Outline each blood parasite and name the species.
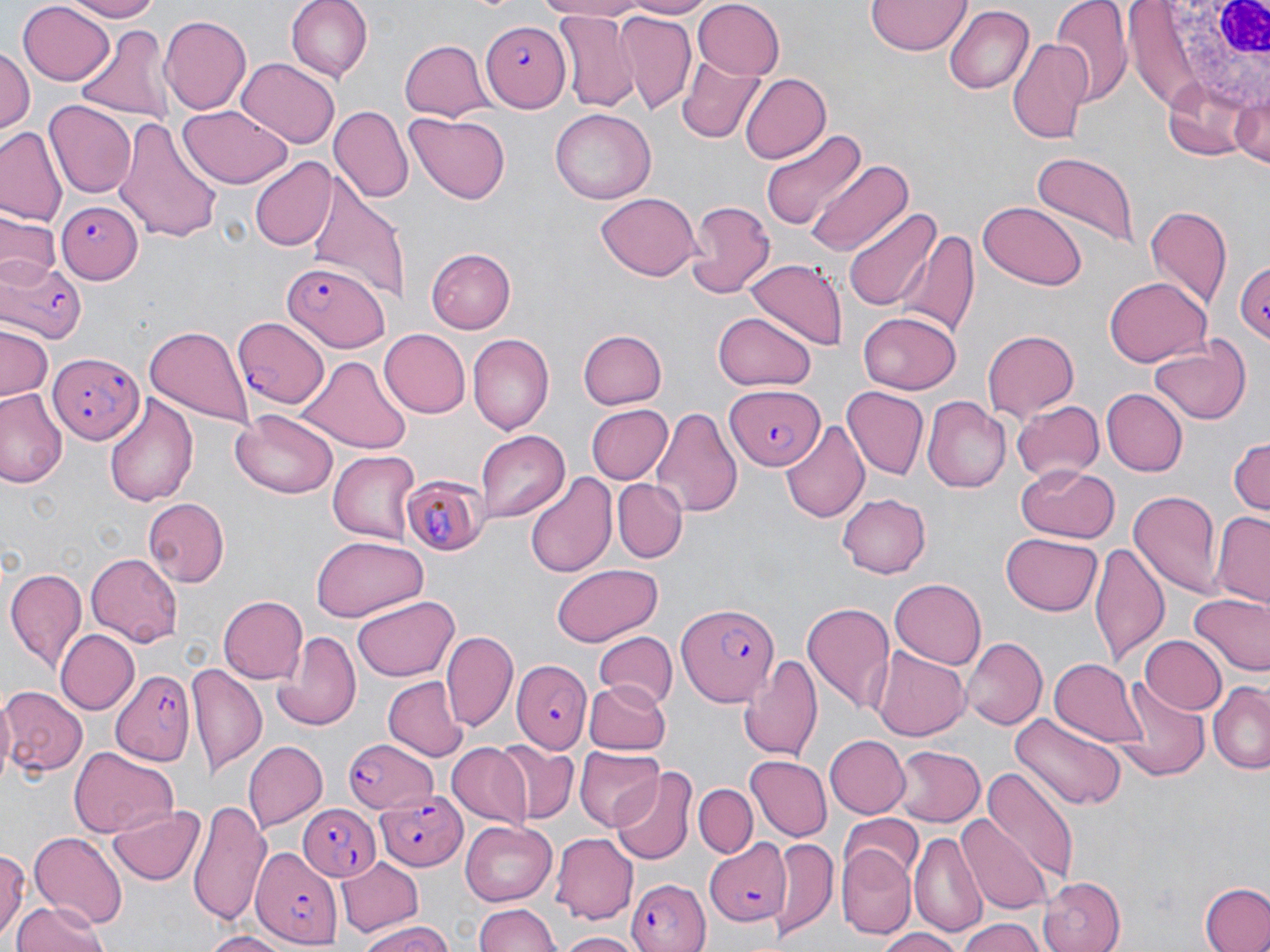

Approximate bounding boxes as [x1, y1, x2, y2] in pixels.
Plasmodium falciparum-infected red blood cells: [482, 21, 571, 111], [56, 201, 142, 283], [0, 255, 86, 344], [1230, 259, 1270, 343], [281, 263, 389, 351], [232, 317, 330, 407], [49, 350, 145, 446], [723, 382, 822, 471], [398, 472, 488, 554], [677, 602, 778, 707], [513, 659, 590, 753], [110, 669, 199, 767], [341, 737, 441, 815], [374, 790, 468, 869], [301, 800, 384, 880], [696, 839, 790, 929], [250, 845, 344, 947], [626, 875, 713, 951].
No Plasmodium ovale, Plasmodium malariae, Plasmodium vivax, Babesia divergens, or Trypanosoma brucei observed.

Summary:
  - Uninfected red blood cell locations: [62, 0, 163, 21], [284, 0, 370, 81], [535, 0, 655, 21], [614, 0, 712, 18], [1053, 0, 1131, 105], [691, 1, 785, 79], [866, 1, 969, 57], [17, 2, 116, 87], [945, 6, 1033, 93], [552, 12, 639, 112], [613, 12, 696, 114], [158, 16, 251, 114], [75, 22, 175, 124], [1006, 37, 1095, 147], [399, 41, 493, 121], [0, 47, 34, 142], [238, 59, 339, 150], [678, 59, 767, 143], [739, 72, 831, 165], [1232, 92, 1270, 170], [44, 101, 136, 197], [181, 104, 289, 187], [330, 107, 413, 205], [550, 107, 655, 206], [114, 113, 221, 243], [406, 113, 511, 205], [760, 125, 867, 233], [0, 127, 65, 224], [1029, 150, 1141, 245], [247, 158, 338, 251], [806, 159, 914, 259], [301, 171, 408, 299], [596, 194, 701, 280], [684, 199, 774, 301], [979, 202, 1087, 291], [1143, 205, 1231, 314], [844, 207, 942, 313], [0, 213, 58, 285], [897, 227, 980, 341], [428, 248, 515, 333], [746, 258, 846, 349], [1105, 277, 1212, 366], [860, 309, 963, 393], [713, 312, 819, 391], [145, 327, 251, 427], [0, 328, 53, 403], [379, 329, 469, 417], [578, 330, 668, 410], [983, 330, 1081, 423], [468, 335, 555, 432], [1149, 337, 1253, 426], [301, 355, 410, 454], [0, 387, 66, 489], [839, 388, 925, 480], [1104, 389, 1187, 475], [104, 394, 198, 506], [923, 398, 1012, 493], [1011, 400, 1102, 483], [584, 404, 672, 485], [652, 407, 742, 520], [231, 411, 337, 499], [778, 416, 869, 525], [475, 431, 571, 523], [1227, 433, 1270, 519], [327, 449, 420, 544], [1017, 464, 1116, 544], [525, 473, 618, 579], [612, 478, 687, 561], [1127, 490, 1224, 598], [836, 492, 930, 577], [144, 498, 228, 584], [1211, 512, 1270, 606], [1001, 533, 1104, 617], [312, 536, 425, 621], [1091, 539, 1168, 669], [87, 553, 181, 647], [550, 563, 663, 645], [4, 567, 86, 670], [891, 577, 988, 669], [1188, 592, 1269, 677], [218, 595, 308, 682], [354, 596, 459, 683], [802, 603, 894, 714], [270, 628, 362, 731], [442, 629, 516, 731], [56, 630, 139, 713], [593, 631, 679, 707], [1138, 634, 1228, 715], [962, 636, 1047, 731], [871, 648, 970, 741], [742, 653, 823, 763], [1051, 657, 1149, 750], [187, 662, 265, 774], [381, 677, 467, 762], [583, 679, 672, 752], [1113, 680, 1209, 782], [1209, 682, 1269, 774], [2, 685, 88, 778], [1012, 712, 1125, 811], [823, 735, 907, 819], [491, 739, 578, 824], [243, 740, 325, 830], [446, 743, 529, 827], [894, 744, 985, 827], [70, 746, 175, 839], [575, 747, 664, 830], [745, 757, 831, 842], [979, 767, 1079, 889], [615, 770, 695, 866], [694, 784, 756, 858], [189, 797, 273, 930], [107, 805, 209, 887], [962, 816, 1055, 914], [838, 817, 923, 887], [459, 819, 556, 908], [27, 831, 128, 928], [910, 831, 986, 941], [553, 833, 638, 922], [767, 836, 838, 938], [838, 846, 917, 936], [0, 848, 27, 943], [336, 856, 422, 935], [1039, 875, 1126, 952], [1200, 881, 1270, 952], [11, 899, 108, 952], [473, 901, 563, 952], [958, 917, 1045, 952], [357, 920, 457, 952], [874, 927, 963, 952], [196, 931, 298, 952], [557, 932, 639, 952]
  - White blood cell locations: [1153, 0, 1269, 119]
  - Slide-level diagnosis: Plasmodium falciparum
  - Image size: 1270×952 pixels
  - Field of view: single
  - Modality: optical microscopy
  - Stain: May-Grünwald-Giemsa
  - Magnification: 1000x
  - Preparation: thin blood smear